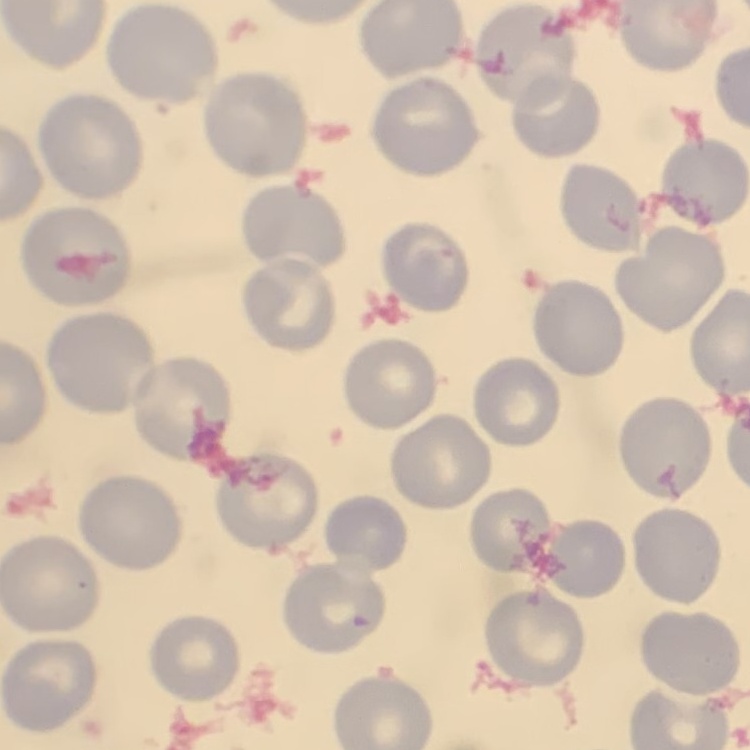

{
  "red_blood_cell_morphology": "no rouleaux formation",
  "stain": "Field's or Giemsa",
  "preparation": "thin peripheral smear",
  "image_type": "one tile cut from a larger photomicrograph"
}